Classify this cell by malaria status.
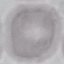

Uninfected.

Summary:
  - Stain: Giemsa
  - Capture: smartphone through the microscope eyepiece
  - Preparation: thin blood smear
  - Image type: cell patch, automatically extracted from a larger field of view and resized to 64 × 64 pixels